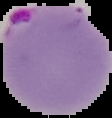
Result: malaria parasites detected. From a thin blood film. Image is 112×118 pixels. The area outside the segmented cell region is set to black.